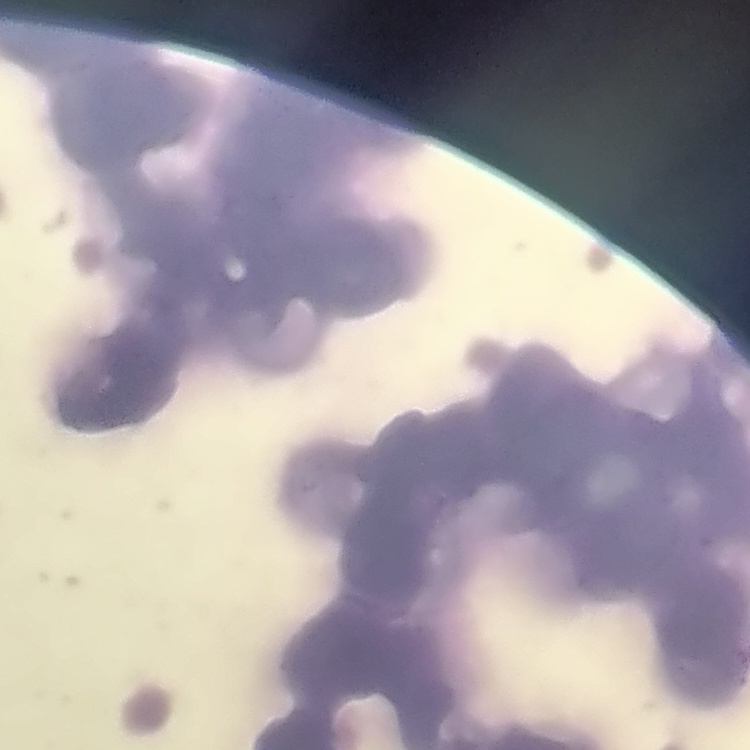

The red blood cells show rouleaux formation. Stained with either Field's or Giemsa. Square crop of a larger photomicrograph. Thin peripheral smear.